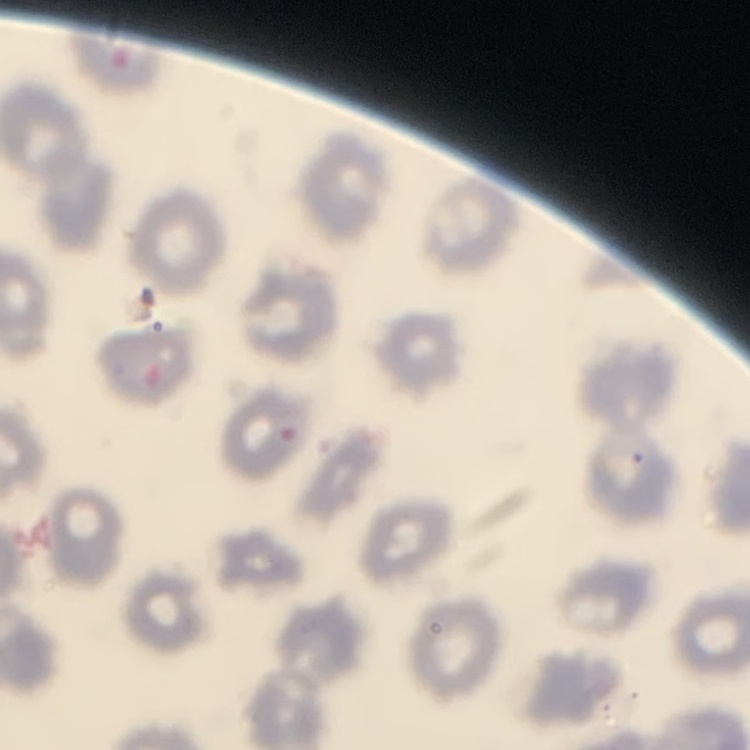

erythrocyte morphology = no rouleaux formation
preparation = thin blood smear
image type = square crop of a larger photomicrograph
stain = Field's or Giemsa